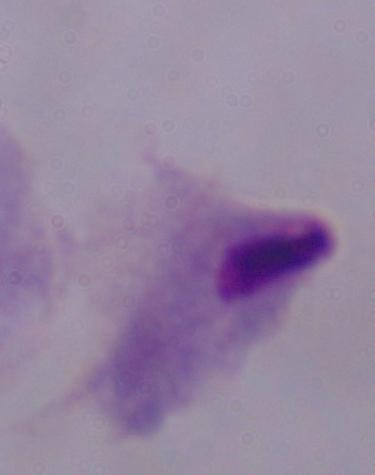

{
  "magnification": "1000x",
  "identification": "trichomonad",
  "modality": "micrograph"
}